Name the parasite shown.
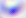

This is Toxoplasma gondii.

modality = micrograph
magnification = 400x